Assess this cell for malaria.
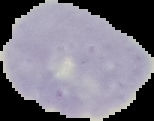
Uninfected.

Summary:
  - Image size: 154×121 pixels
  - Preparation: thin blood film
  - Image type: segmented cell region with the area outside set to black